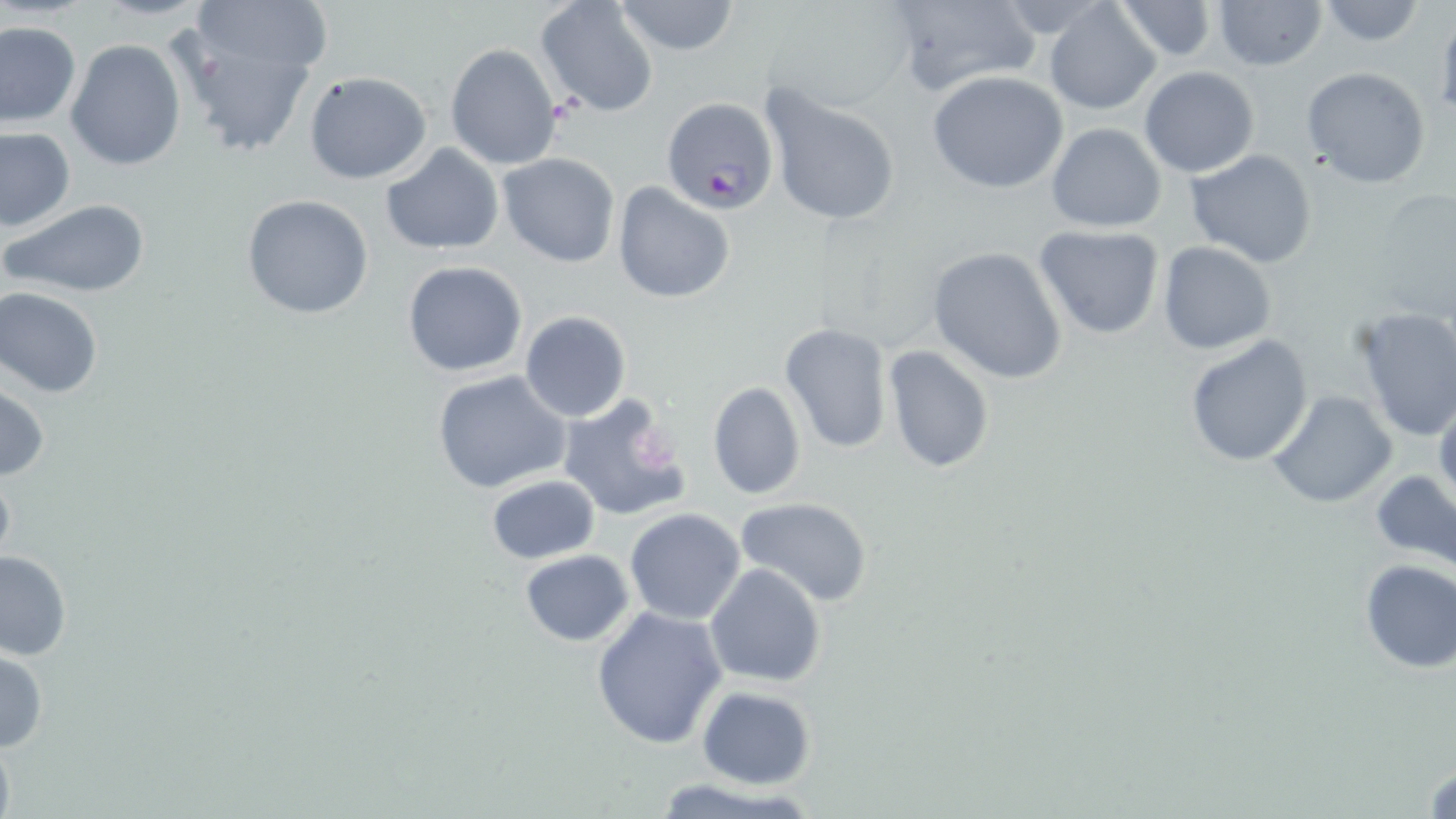

Plasmodium falciparum-infected red blood cell locations = approximate bounding boxes as named x1/y1/x2/y2 corners in pixels: (x1=662, y1=95, x2=779, y2=213)
slide-level diagnosis = Plasmodium falciparum
platelet locations = approximate bounding boxes as named x1/y1/x2/y2 corners in pixels: (x1=631, y1=427, x2=682, y2=477)
field of view = single
stain = May-Grünwald-Giemsa
preparation = thin blood film
modality = light microscopy
uninfected red blood cell locations = approximate bounding boxes as named x1/y1/x2/y2 corners in pixels: (x1=195, y1=0, x2=332, y2=75), (x1=535, y1=0, x2=658, y2=118), (x1=612, y1=0, x2=743, y2=56), (x1=887, y1=0, x2=1041, y2=97), (x1=1110, y1=0, x2=1220, y2=62), (x1=1211, y1=0, x2=1327, y2=70), (x1=1313, y1=0, x2=1427, y2=47), (x1=1043, y1=2, x2=1161, y2=115), (x1=0, y1=21, x2=81, y2=127), (x1=170, y1=30, x2=320, y2=159), (x1=66, y1=39, x2=186, y2=172), (x1=445, y1=42, x2=563, y2=171), (x1=1139, y1=66, x2=1261, y2=178), (x1=1302, y1=66, x2=1433, y2=189), (x1=927, y1=70, x2=1070, y2=194), (x1=303, y1=71, x2=433, y2=185), (x1=760, y1=87, x2=903, y2=227), (x1=1045, y1=123, x2=1166, y2=232), (x1=0, y1=124, x2=75, y2=230), (x1=380, y1=143, x2=505, y2=255), (x1=1185, y1=148, x2=1318, y2=268), (x1=497, y1=153, x2=621, y2=268), (x1=613, y1=182, x2=735, y2=305), (x1=241, y1=194, x2=375, y2=320), (x1=3, y1=197, x2=151, y2=298), (x1=1033, y1=226, x2=1166, y2=341), (x1=1156, y1=242, x2=1276, y2=354), (x1=928, y1=246, x2=1068, y2=384), (x1=402, y1=260, x2=529, y2=378), (x1=0, y1=287, x2=104, y2=398), (x1=1349, y1=305, x2=1456, y2=441), (x1=519, y1=310, x2=631, y2=423), (x1=778, y1=322, x2=893, y2=454), (x1=1184, y1=334, x2=1313, y2=468), (x1=882, y1=344, x2=995, y2=475), (x1=430, y1=370, x2=573, y2=495), (x1=0, y1=381, x2=49, y2=483), (x1=706, y1=382, x2=807, y2=500), (x1=1266, y1=389, x2=1397, y2=509), (x1=556, y1=394, x2=689, y2=523), (x1=1433, y1=394, x2=1456, y2=510), (x1=0, y1=466, x2=16, y2=575), (x1=1372, y1=472, x2=1456, y2=569), (x1=484, y1=475, x2=602, y2=565), (x1=733, y1=497, x2=876, y2=606), (x1=624, y1=508, x2=746, y2=625), (x1=0, y1=549, x2=73, y2=661), (x1=519, y1=549, x2=635, y2=647), (x1=1358, y1=559, x2=1455, y2=672), (x1=704, y1=562, x2=827, y2=689), (x1=591, y1=605, x2=728, y2=749), (x1=0, y1=649, x2=49, y2=753), (x1=697, y1=686, x2=816, y2=789), (x1=1422, y1=755, x2=1455, y2=817)
image size = 1456×819 pixels
magnification = 1000x